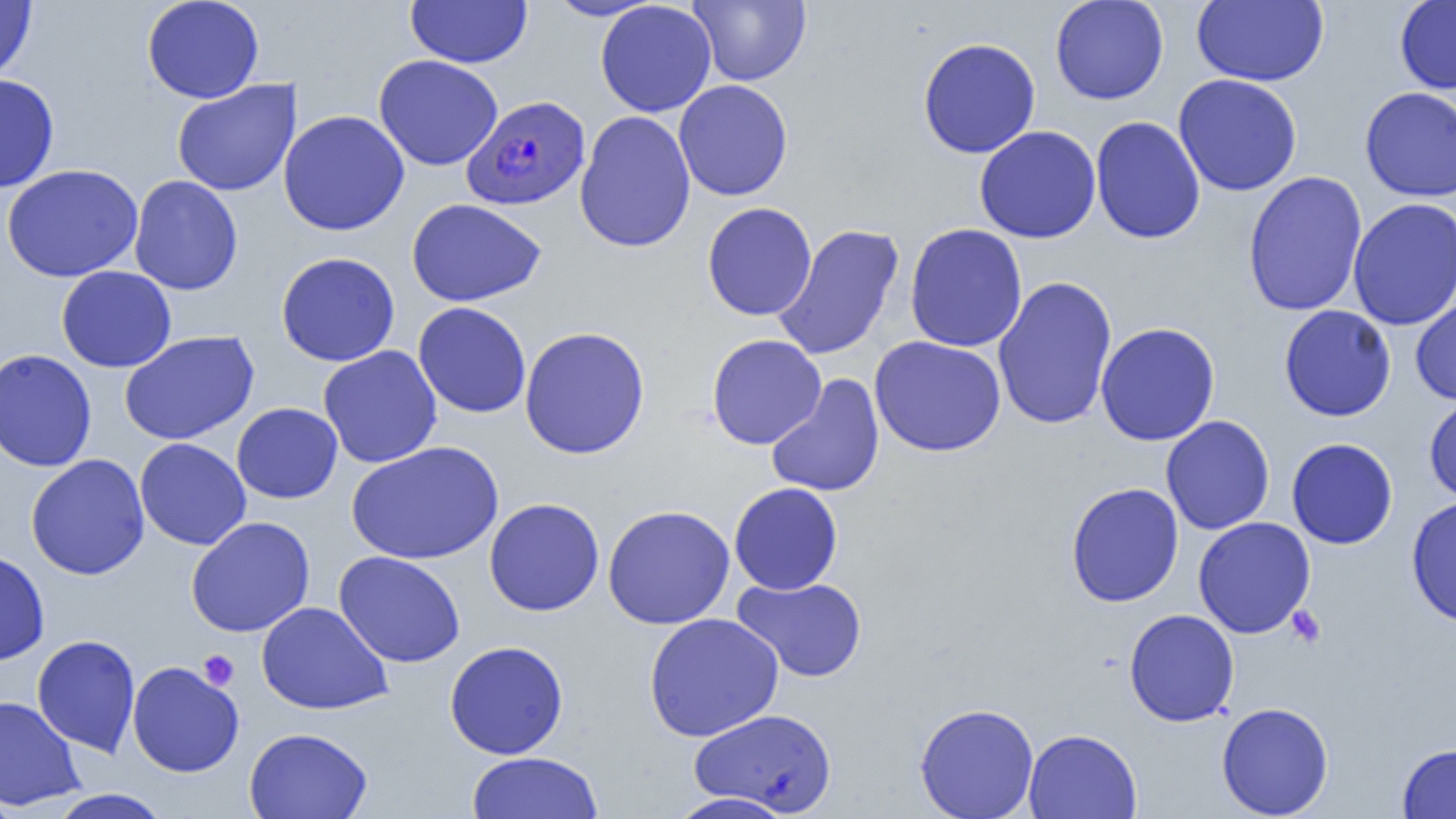

slide_level_diagnosis: Plasmodium falciparum
field_of_view: one of a larger specimen
preparation: thin blood film
image_size: 1456×819 pixels
platelet_locations: 'approximate bounding boxes as (x1, y1, x2, y2) in pixels: (1286, 605, 1326, 648), (198, 650, 239, 690)'
modality: optical microscopy
plasmodium_falciparum_infected_red_blood_cell_locations: 'approximate bounding boxes as (x1, y1, x2, y2) in pixels: (462, 95, 591, 210)'
uninfected_red_blood_cell_locations: 'approximate bounding boxes as (x1, y1, x2, y2) in pixels: (0, 0, 37, 83), (141, 0, 264, 103), (405, 0, 532, 68), (546, 0, 662, 21), (687, 0, 811, 87), (1049, 0, 1169, 105), (1191, 0, 1328, 87), (1394, 0, 1456, 95), (595, 1, 717, 117), (917, 38, 1042, 158), (374, 54, 503, 171), (0, 74, 60, 192), (1173, 74, 1303, 197), (171, 79, 301, 196), (674, 79, 793, 201), (1359, 87, 1456, 202), (278, 109, 410, 236), (575, 111, 696, 253), (1090, 116, 1206, 244), (974, 125, 1101, 244), (2, 164, 144, 282), (1242, 171, 1368, 316), (129, 175, 243, 295), (1347, 197, 1456, 331), (406, 198, 546, 307), (702, 203, 817, 321), (904, 223, 1028, 352), (772, 224, 904, 361), (275, 251, 401, 367), (56, 265, 177, 372), (992, 276, 1118, 430), (1410, 288, 1456, 406), (412, 301, 531, 418), (1278, 305, 1397, 422), (1095, 322, 1220, 446), (519, 326, 650, 459), (119, 330, 259, 445), (706, 334, 826, 449), (869, 335, 1007, 457), (318, 345, 442, 468), (0, 349, 97, 472), (766, 374, 885, 498), (1423, 393, 1456, 505), (231, 402, 343, 504), (1160, 415, 1275, 534), (135, 437, 251, 551), (1286, 437, 1398, 550), (345, 440, 505, 565), (25, 455, 150, 580), (728, 482, 843, 595), (1065, 482, 1184, 608), (1405, 495, 1456, 627), (484, 497, 605, 616), (602, 504, 736, 629), (186, 516, 315, 637), (1193, 516, 1315, 639), (0, 549, 50, 665), (333, 550, 466, 668), (732, 576, 868, 683), (256, 601, 393, 716), (1123, 609, 1240, 727), (643, 613, 784, 741), (32, 635, 140, 757), (444, 641, 568, 759), (127, 661, 244, 777), (0, 695, 86, 810), (1216, 701, 1334, 818), (914, 702, 1039, 819), (689, 708, 837, 815), (243, 727, 374, 819), (1023, 728, 1142, 819), (1396, 742, 1456, 819), (466, 751, 603, 818), (0, 787, 19, 819), (48, 788, 171, 819), (667, 792, 797, 819)'
magnification: 1000x